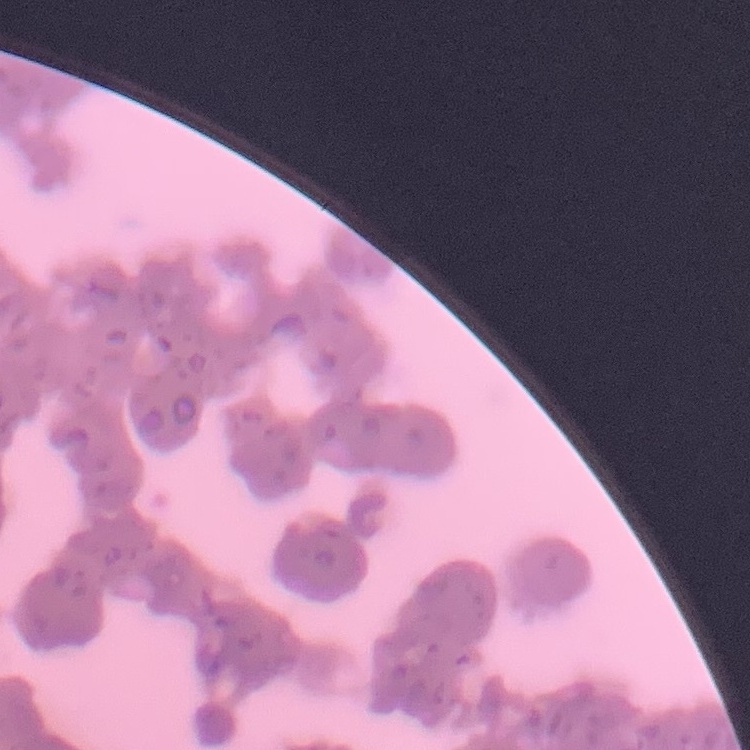
Summary:
  - Erythrocyte morphology: rouleaux formation
  - Preparation: thin peripheral smear
  - Stain: Field's or Giemsa
  - Image type: square crop of a larger photomicrograph